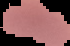

Segmented cell region on a black background. Malaria status: parasitized. Image is 70×46 pixels. From a thin blood smear.